Locate every blood parasite and identify its species.
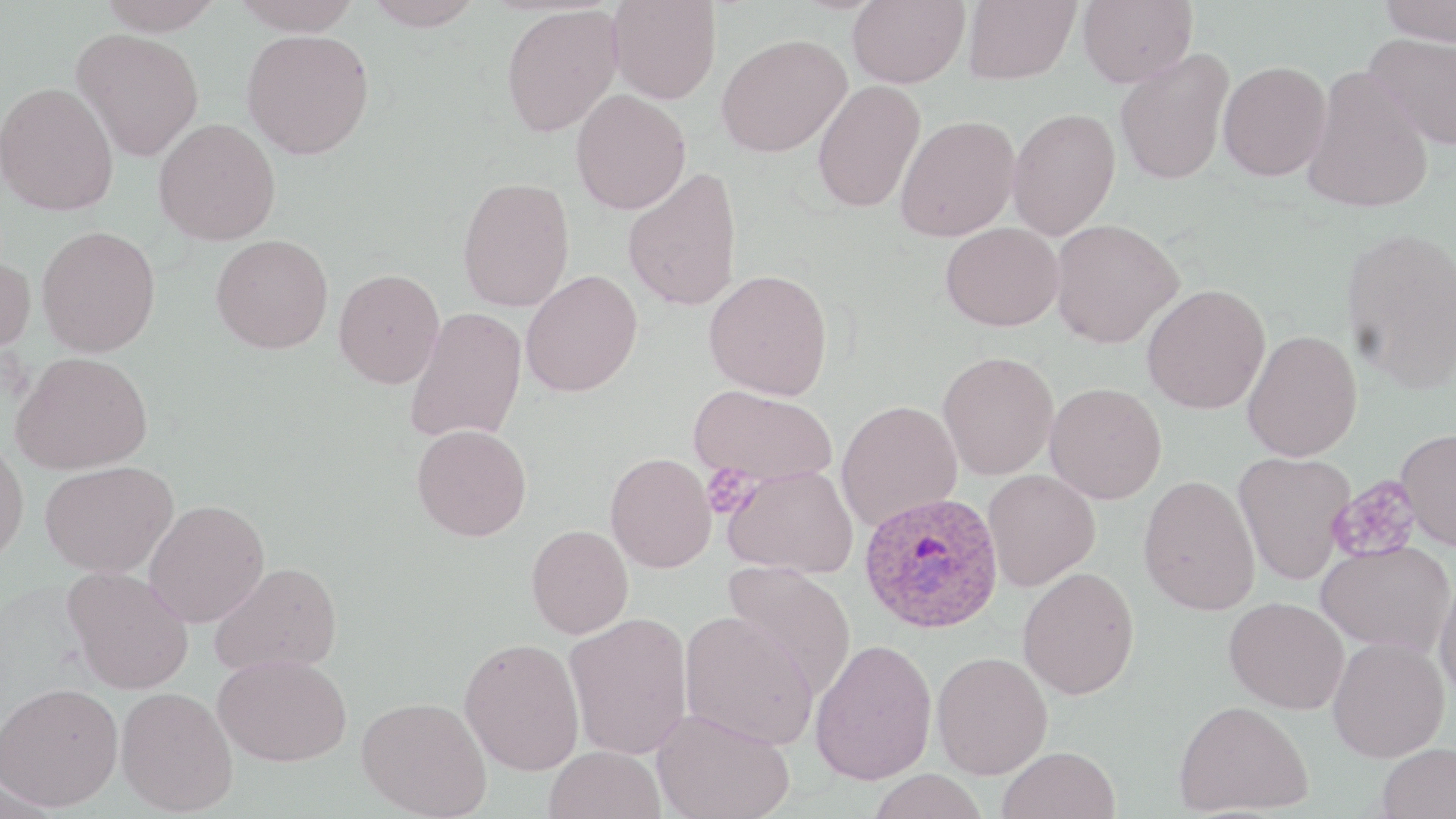

Approximate bounding boxes as (x1, y1, x2, y2) in pixels.
Plasmodium ovale-infected red blood cells: (859, 491, 1004, 634).
No Plasmodium falciparum, Plasmodium malariae, Plasmodium vivax, Babesia divergens, or Trypanosoma brucei observed.

Platelet locations: (701, 464, 758, 518), (1328, 476, 1423, 563). Uninfected red blood cell locations: (97, 0, 225, 35), (231, 0, 363, 35), (363, 0, 485, 30), (848, 0, 969, 88), (962, 0, 1081, 84), (1078, 0, 1198, 87), (1378, 0, 1456, 45), (608, 1, 721, 104), (500, 4, 623, 138), (72, 28, 205, 162), (241, 29, 375, 159), (1363, 31, 1456, 152), (716, 33, 851, 157), (1115, 49, 1234, 185), (1217, 60, 1332, 181), (1301, 65, 1434, 214), (812, 80, 925, 214), (0, 81, 118, 216), (571, 90, 691, 215), (1007, 107, 1120, 240), (895, 115, 1021, 242), (153, 117, 281, 245), (622, 167, 743, 311), (457, 176, 575, 312), (1048, 218, 1184, 348), (940, 222, 1064, 331), (36, 224, 161, 357), (1341, 226, 1456, 393), (211, 234, 333, 354), (0, 252, 36, 356), (333, 268, 444, 389), (521, 269, 643, 397), (704, 269, 833, 401), (1142, 284, 1271, 413), (405, 307, 528, 445), (1242, 329, 1362, 461), (938, 350, 1058, 480), (11, 351, 153, 475), (1045, 382, 1167, 504), (689, 384, 837, 488), (836, 399, 963, 532), (411, 423, 532, 541), (1395, 427, 1456, 551), (0, 439, 29, 565), (1233, 451, 1354, 585), (606, 452, 717, 573), (40, 460, 179, 578), (722, 464, 858, 577), (982, 470, 1101, 591), (1138, 474, 1261, 615), (143, 499, 270, 627), (526, 524, 634, 639), (1316, 540, 1454, 655), (210, 561, 343, 675), (723, 562, 856, 698), (64, 566, 194, 695), (1017, 567, 1140, 700), (1434, 569, 1456, 705), (1224, 596, 1349, 714), (680, 610, 819, 750), (565, 613, 693, 759), (1328, 636, 1450, 762), (459, 637, 585, 776), (810, 638, 937, 785), (932, 651, 1053, 779), (213, 653, 353, 766), (0, 682, 124, 810), (115, 687, 238, 815), (357, 696, 491, 818), (1174, 699, 1313, 816), (652, 708, 795, 819), (1377, 742, 1456, 818), (544, 745, 666, 819), (998, 745, 1120, 819), (867, 768, 988, 819). Slide-level diagnosis: Plasmodium ovale. 1000x magnification. Optical microscopy. Thin blood film. One field of a larger specimen. Image is 1456×819 pixels. May-Grünwald-Giemsa-stained preparation.